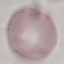
result = no malaria parasites detected
preparation = thin blood smear
stain = Giemsa
capture = smartphone camera at the microscope eyepiece
image type = automatically extracted cell patch, resized to 64 × 64 pixels